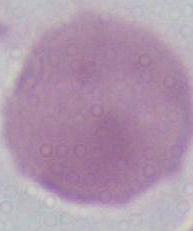
Summary:
  - Magnification: 1000x
  - Modality: micrograph
  - Identification: erythrocyte